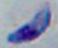

magnification = 1000x
modality = micrograph
identification = Toxoplasma gondii